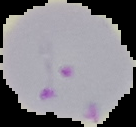
Summary:
  - Malaria status: parasitized
  - Image type: cell region segmented out of the field of view; surrounding area masked to black
  - Image size: 136×127 pixels
  - Preparation: thin blood smear